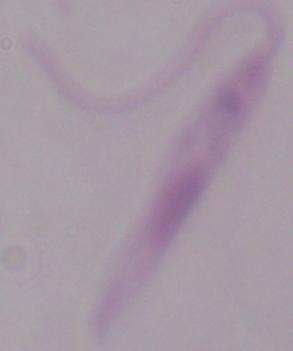
A Leishmania parasite is seen. Micrograph. 1000x magnification.